Assess this cell for malaria.
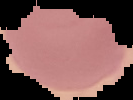

It is uninfected.

Summary:
  - Preparation: thin blood film
  - Image type: cell region segmented out of the field of view; surrounding area masked to black
  - Image size: 133×100 pixels